Name the cell type shown.
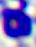
This is a leukocyte.

modality = micrograph
magnification = 400x